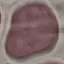
Malaria status: uninfected. Giemsa-stained preparation. Photographed with a smartphone camera at the microscope eyepiece. Cell patch, automatically extracted from a larger field of view and resized to 64 × 64 pixels. Thin blood smear.